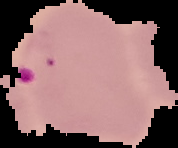

Image is 178×148 pixels. The area outside the segmented cell region is set to black. Result: malaria parasites detected. From a thin blood film.